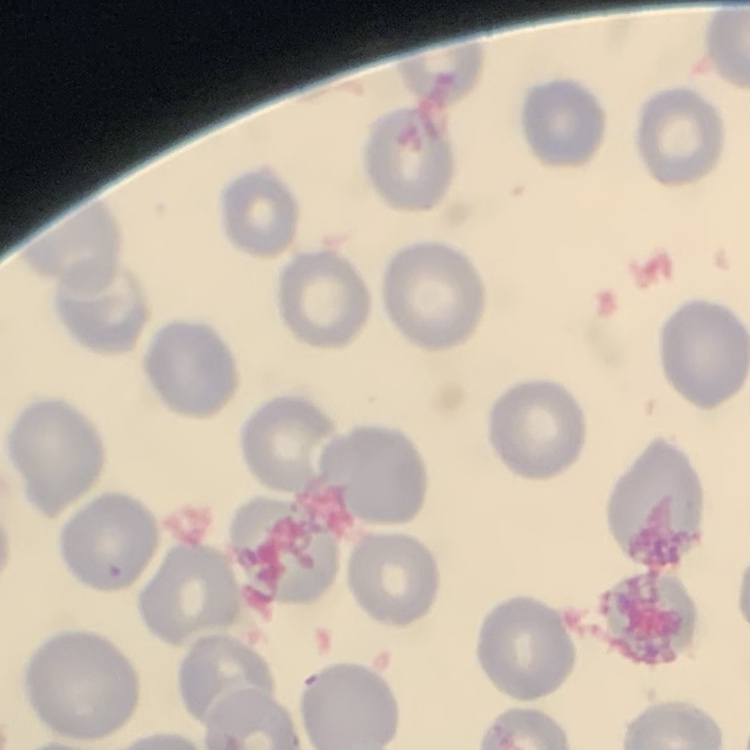
The erythrocytes show no rouleaux formation. Square crop of a larger photomicrograph. Thin blood smear. Stained with either Field's or Giemsa.